State which parasite is depicted.
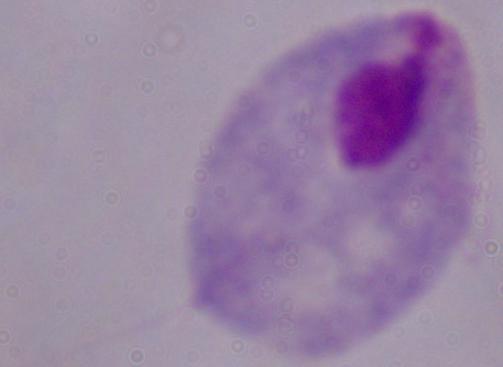

This is a trichomonad.

magnification = 1000x
modality = photomicrograph